Identify the parasite.
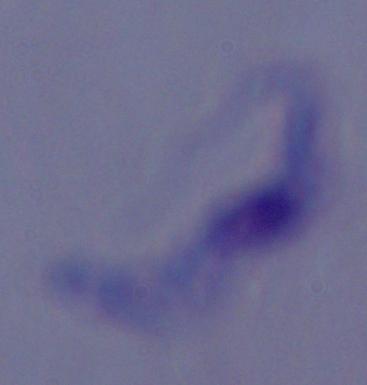
A trypanosome.

modality: micrograph
magnification: 1000x